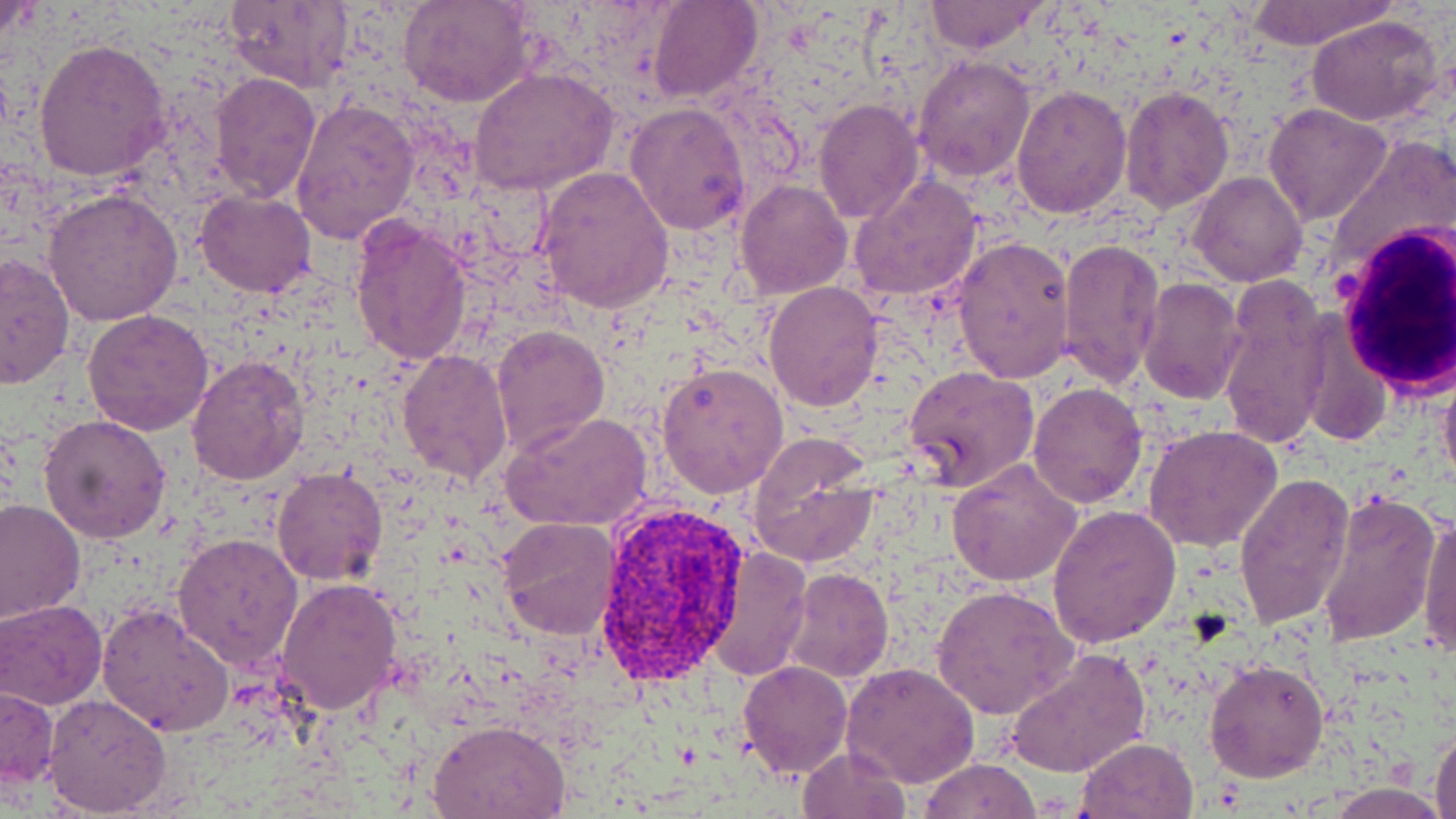 Approximate bounding boxes as (x1, y1, x2, y2) in pixels. White blood cell locations: (1333, 225, 1456, 394). Plasmodium vivax-infected red blood cell locations: (593, 508, 751, 683). Uninfected red blood cell locations: (0, 0, 45, 51), (399, 0, 534, 108), (647, 0, 763, 105), (1244, 0, 1394, 50), (223, 1, 355, 92), (923, 1, 1047, 55), (1307, 15, 1446, 126), (33, 37, 170, 182), (913, 54, 1036, 182), (470, 67, 619, 198), (209, 73, 321, 205), (1010, 86, 1132, 218), (1120, 86, 1233, 211), (291, 97, 419, 243), (813, 98, 924, 225), (625, 101, 752, 234), (1264, 103, 1391, 224), (535, 166, 673, 313), (1188, 171, 1308, 288), (849, 176, 984, 304), (735, 179, 851, 299), (42, 187, 185, 326), (194, 191, 317, 298), (349, 215, 472, 367), (952, 235, 1075, 382), (1058, 237, 1166, 389), (0, 253, 74, 390), (1215, 275, 1332, 455), (1136, 277, 1245, 406), (763, 281, 886, 411), (82, 308, 214, 435), (1296, 316, 1391, 449), (491, 322, 609, 454), (396, 348, 513, 485), (188, 355, 309, 485), (657, 363, 788, 499), (1438, 363, 1456, 495), (903, 366, 1038, 492), (1027, 381, 1147, 507), (503, 411, 652, 533), (38, 414, 171, 544), (1144, 423, 1282, 553), (745, 434, 878, 568), (944, 457, 1083, 588), (273, 465, 388, 586), (1233, 472, 1355, 629), (1313, 489, 1441, 647), (0, 499, 84, 622), (1048, 505, 1181, 648), (1418, 508, 1456, 657), (497, 516, 621, 640), (173, 532, 304, 671), (705, 548, 811, 680), (785, 567, 893, 683), (276, 578, 403, 716), (934, 585, 1079, 721), (1, 599, 107, 708), (96, 603, 234, 736), (1005, 645, 1153, 779), (1205, 659, 1329, 783), (738, 660, 852, 778), (842, 661, 981, 789), (1, 685, 59, 790), (44, 694, 171, 817), (430, 718, 572, 818), (1430, 726, 1456, 819), (1075, 737, 1199, 818), (797, 746, 911, 819), (919, 758, 1040, 819). Slide-level diagnosis: Plasmodium vivax. May-Grünwald-Giemsa-stained preparation. One field of a larger specimen. Thin blood film. Captured at 1000x magnification. Light microscopy. Image is 1456×819 pixels.